Classify this cell by malaria status.
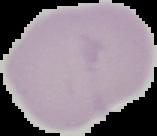

Uninfected.

image type = segmented cell region on a black background
image size = 157×136 pixels
preparation = thin blood film